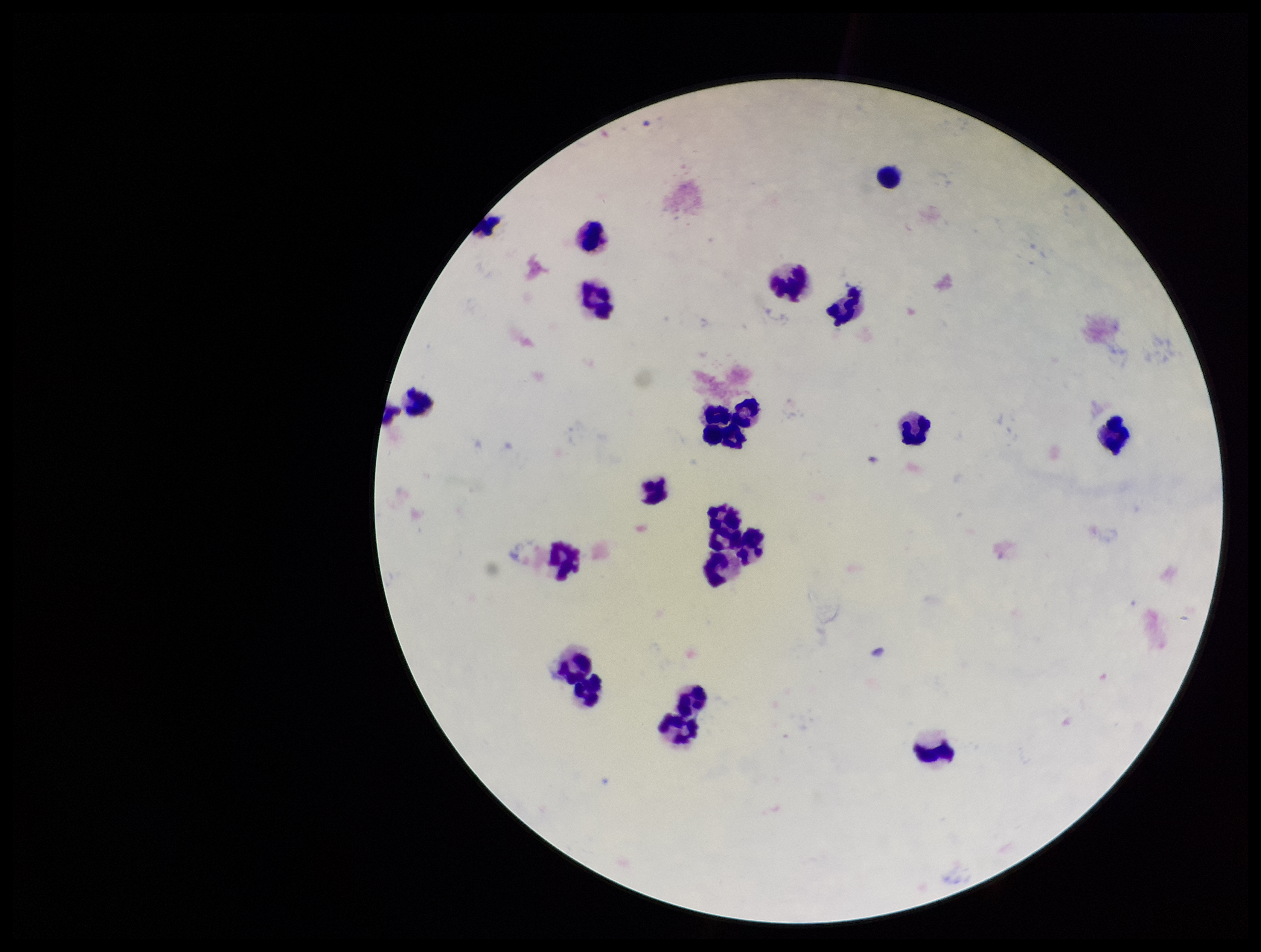

image size = 1261×952 pixels
patient malaria status = negative
Plasmodium parasites = none seen
preparation = thick
capture = smartphone photograph through the microscope eyepiece
stain = Giemsa
field of view = single
leukocyte count = 22
parasite count = 0